Report the malaria status of this cell.
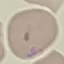
Parasitized.

Acquired by smartphone through the microscope eyepiece. Cell patch, automatically extracted from a larger field of view and resized to 64 × 64 pixels. Thin smear of blood. Giemsa-stained preparation.